Point out every Plasmodium parasite and every leukocyte.
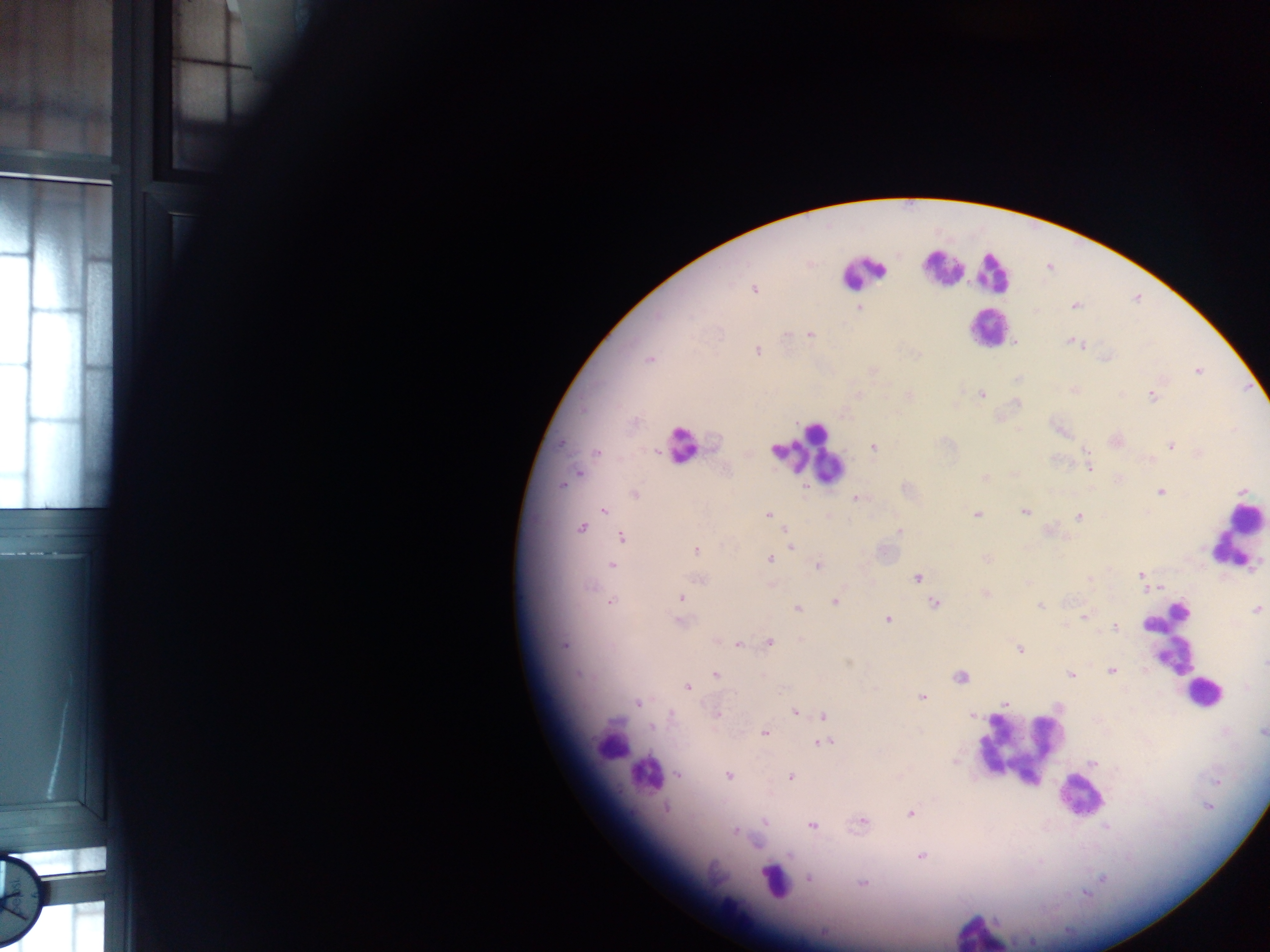
Approximate centers as {x, y} in pixels.
Plasmodium parasites: {754, 289}, {1075, 305}, {858, 307}, {786, 334}, {809, 335}, {1073, 342}, {1016, 343}, {757, 351}, {649, 359}, {1197, 372}, {1075, 390}, {982, 394}, {1152, 396}, {561, 443}, {1171, 445}, {874, 446}, {596, 452}, {655, 452}, {1090, 468}, {578, 473}, {984, 477}, {562, 485}, {1160, 491}, {635, 494}, {856, 498}, {603, 510}, {1025, 511}, {976, 514}, {768, 515}, {1078, 516}, {582, 528}, {899, 531}, {621, 538}, {788, 543}, {791, 547}, {696, 550}, {986, 558}, {770, 559}, {611, 564}, {818, 566}, {1141, 575}, {918, 577}, {698, 579}, {1089, 579}, {986, 594}, {681, 598}, {611, 602}, {835, 602}, {935, 604}, {1040, 606}, {798, 608}, {1256, 610}, {1084, 618}, {888, 620}, {679, 621}, {1115, 628}, {768, 643}, {738, 644}, {564, 645}, {1020, 650}, {1265, 663}, {1112, 670}, {579, 674}, {1071, 674}, {715, 675}, {960, 676}, {687, 687}, {922, 697}, {638, 702}, {1005, 703}, {794, 712}, {716, 714}, {671, 715}, {823, 715}, {971, 715}, {652, 727}, {1263, 730}, {765, 732}, {825, 743}, {955, 762}, {1093, 762}, {678, 775}, {728, 776}, {791, 777}, {666, 808}, {910, 814}, {764, 821}, {862, 822}, {811, 826}, {1106, 826}, {735, 832}, {790, 855}, {922, 856}, {809, 878}, {862, 883}.
Leukocytes: {943, 269}, {862, 271}, {992, 272}, {986, 328}, {684, 442}, {805, 455}, {1241, 523}, {1170, 640}, {1202, 693}, {609, 742}, {1018, 749}, {643, 775}, {1079, 797}, {772, 880}, {980, 932}.

Photographed through a microscope with a mobile-phone camera. Thick blood smear. Image is 1270×952 pixels. Collected in Ghana. Single field of view.